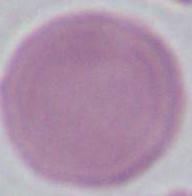
magnification = 1000x
identification = red blood cell
modality = micrograph